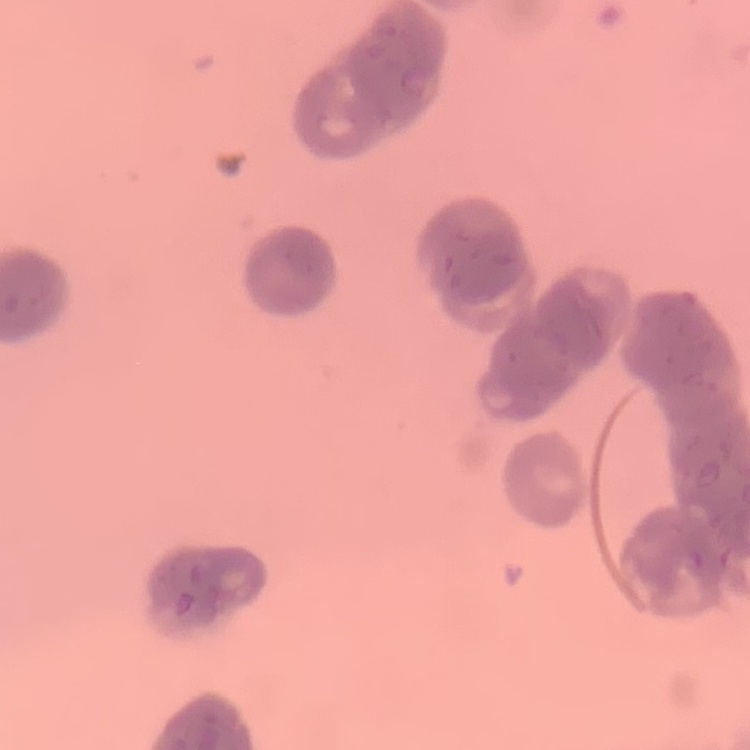 The erythrocytes exhibit rouleaux formation. Thin peripheral smear. One tile cut from a larger photomicrograph. Field's or Giemsa stain.